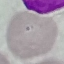

{
  "result": "negative for malaria parasites",
  "capture": "smartphone through the microscope eyepiece",
  "image_type": "automatically extracted cell patch, resized to 64 × 64 pixels",
  "preparation": "thin blood smear",
  "stain": "Giemsa"
}